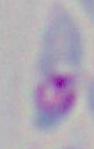

Summary:
  - Modality: photomicrograph
  - Magnification: 1000x
  - Identification: Toxoplasma gondii